State which parasite is depicted.
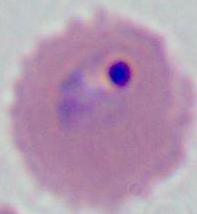
This is Plasmodium.

Micrograph. Captured at either 400x or 1000x magnification.